Name the parasite shown.
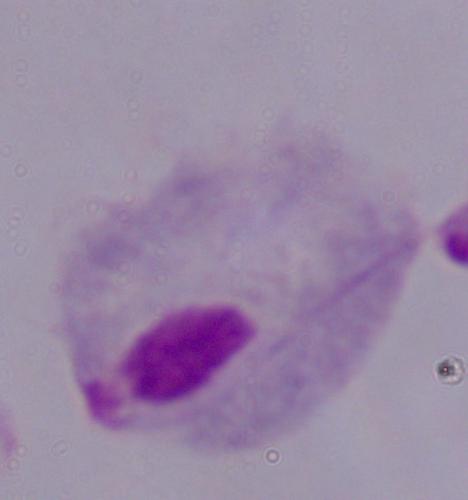
A trichomonad.

Photomicrograph. Captured at 1000x magnification.